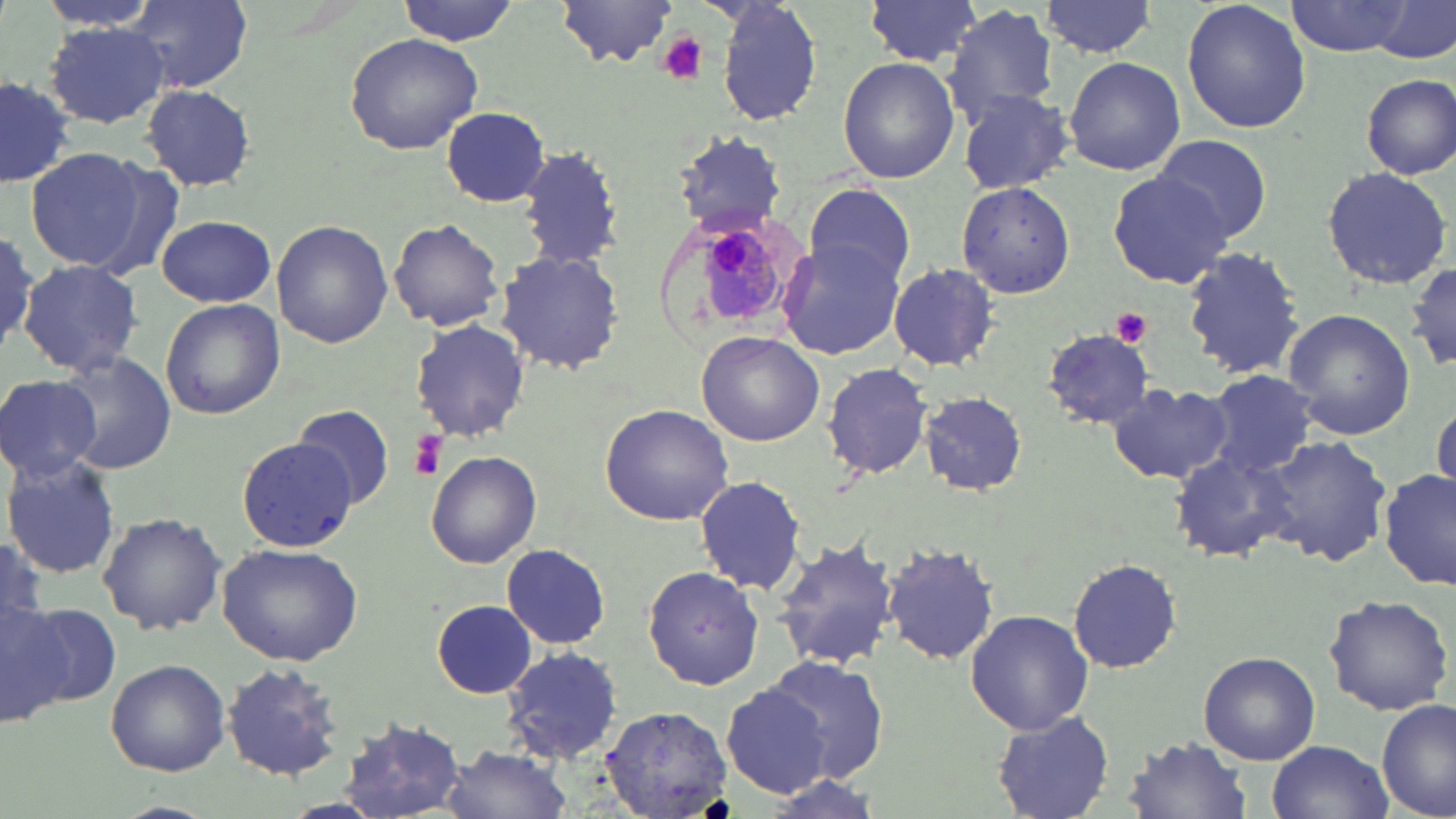
slide-level diagnosis = Plasmodium malariae
image size = 1456×819 pixels
field of view = single
modality = light microscopy
platelet locations = approximate bounding boxes as [x1, y1, x2, y2] in pixels: [655, 32, 710, 86], [1111, 309, 1152, 346], [405, 431, 446, 480]
preparation = thin blood smear
Plasmodium malariae-infected red blood cell locations = approximate bounding boxes as [x1, y1, x2, y2] in pixels: [694, 217, 791, 329]
uninfected red blood cell locations = approximate bounding boxes as [x1, y1, x2, y2] in pixels: [34, 0, 165, 38], [124, 0, 254, 95], [396, 0, 519, 45], [711, 0, 824, 126], [861, 0, 987, 67], [1180, 0, 1313, 136], [1281, 0, 1424, 58], [1038, 1, 1163, 58], [1367, 1, 1455, 64], [556, 2, 684, 70], [945, 5, 1061, 126], [43, 22, 169, 129], [343, 32, 482, 155], [1063, 56, 1184, 175], [838, 57, 960, 183], [1359, 73, 1456, 179], [0, 75, 76, 190], [140, 83, 259, 192], [955, 88, 1074, 195], [441, 106, 550, 207], [675, 131, 784, 235], [1153, 135, 1272, 242], [513, 142, 625, 273], [24, 146, 158, 275], [1320, 167, 1453, 290], [1106, 171, 1237, 290], [957, 180, 1075, 298], [807, 185, 915, 288], [156, 214, 277, 307], [387, 218, 504, 331], [0, 220, 50, 359], [272, 220, 394, 347], [778, 243, 907, 362], [1180, 244, 1308, 381], [496, 248, 625, 376], [18, 260, 146, 379], [1408, 260, 1456, 374], [888, 262, 999, 371], [160, 299, 286, 421], [1283, 310, 1414, 438], [411, 320, 531, 441], [1042, 329, 1160, 430], [696, 330, 824, 446], [55, 350, 178, 473], [822, 360, 937, 481], [1205, 369, 1319, 478], [0, 373, 104, 481], [1107, 382, 1232, 485], [1429, 391, 1456, 504], [918, 393, 1027, 495], [291, 403, 396, 508], [600, 403, 734, 526], [1262, 435, 1392, 568], [236, 438, 358, 553], [1169, 450, 1296, 562], [426, 452, 541, 567], [4, 455, 121, 579], [1379, 468, 1456, 592], [694, 475, 806, 595], [97, 511, 226, 636], [773, 536, 901, 670], [217, 542, 365, 666], [501, 543, 612, 649], [881, 543, 1000, 665], [1069, 558, 1181, 673], [0, 560, 65, 730], [641, 566, 765, 690], [1324, 593, 1452, 717], [14, 596, 119, 716], [432, 599, 536, 699], [965, 611, 1093, 734], [503, 647, 625, 762], [1198, 651, 1321, 764], [761, 655, 888, 783], [106, 658, 230, 776], [221, 661, 349, 783], [718, 682, 835, 800], [1378, 700, 1455, 819], [598, 703, 736, 819], [991, 710, 1115, 818], [334, 718, 470, 818], [1125, 737, 1252, 818], [1267, 739, 1393, 819], [436, 745, 577, 819]
stain = May-Grünwald-Giemsa
magnification = 1000x